Assess this cell for malaria.
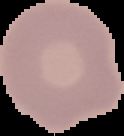
It is uninfected.

Cell region segmented out of the field of view; the surrounding area is masked to black. From a thin blood smear. Image is 124×136 pixels.